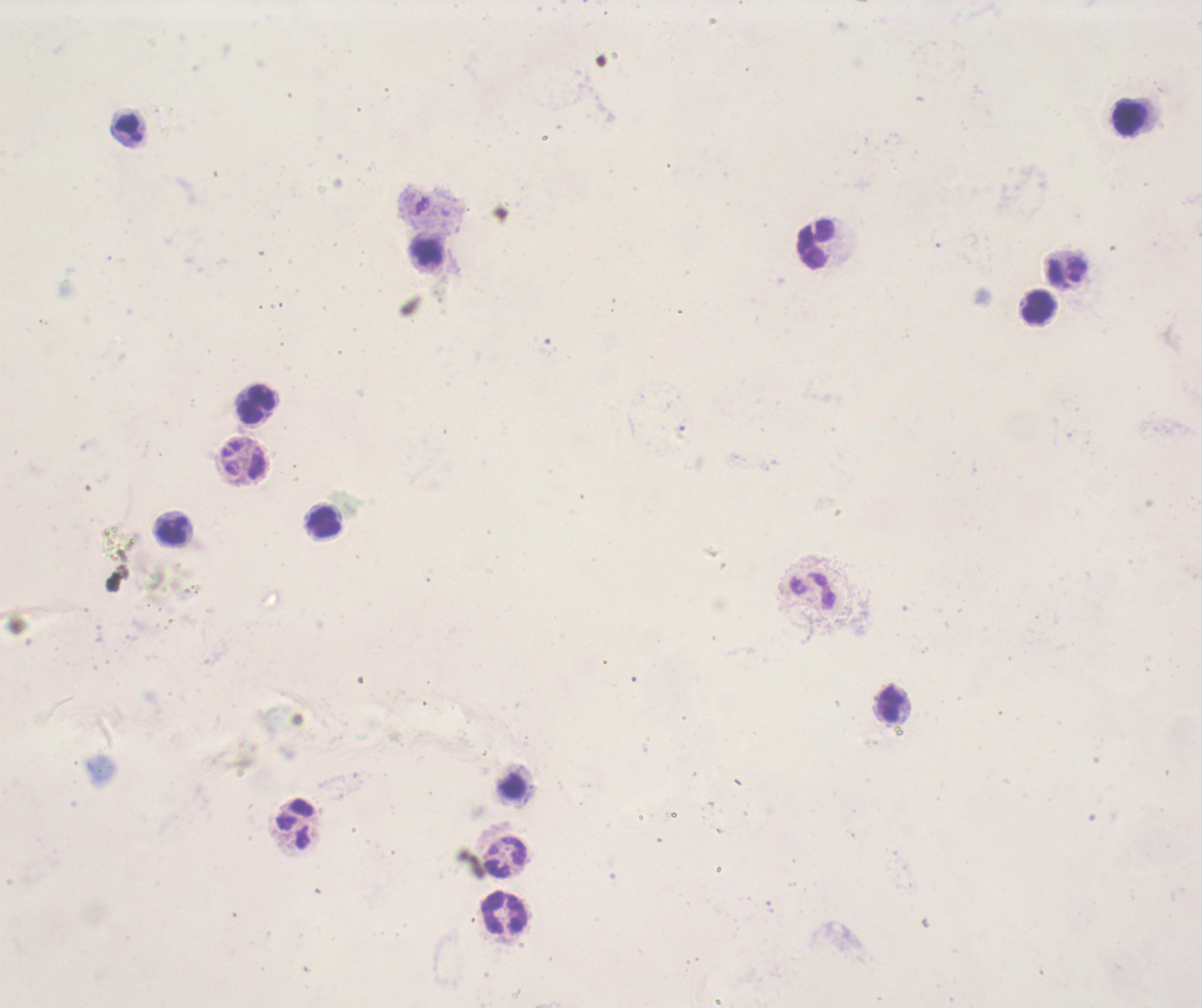

Approximate centers as {x, y} in pixels.
Summary:
  - Leukocyte locations: {1129, 119}, {816, 245}, {1067, 272}, {1038, 307}, {256, 406}, {322, 521}, {891, 705}, {295, 824}, {505, 858}, {504, 912}
  - Magnification: 100x
  - Coloration quality: bad
  - Image size: 1202×1008 pixels
  - Preparation: thick blood smear
  - Stain: Romanowsky
  - Background quality: unsatisfactory
  - Field of view: single
  - Result: no malaria parasites seen
  - Context: previously used in an actual diagnosis